Point out each leukocyte.
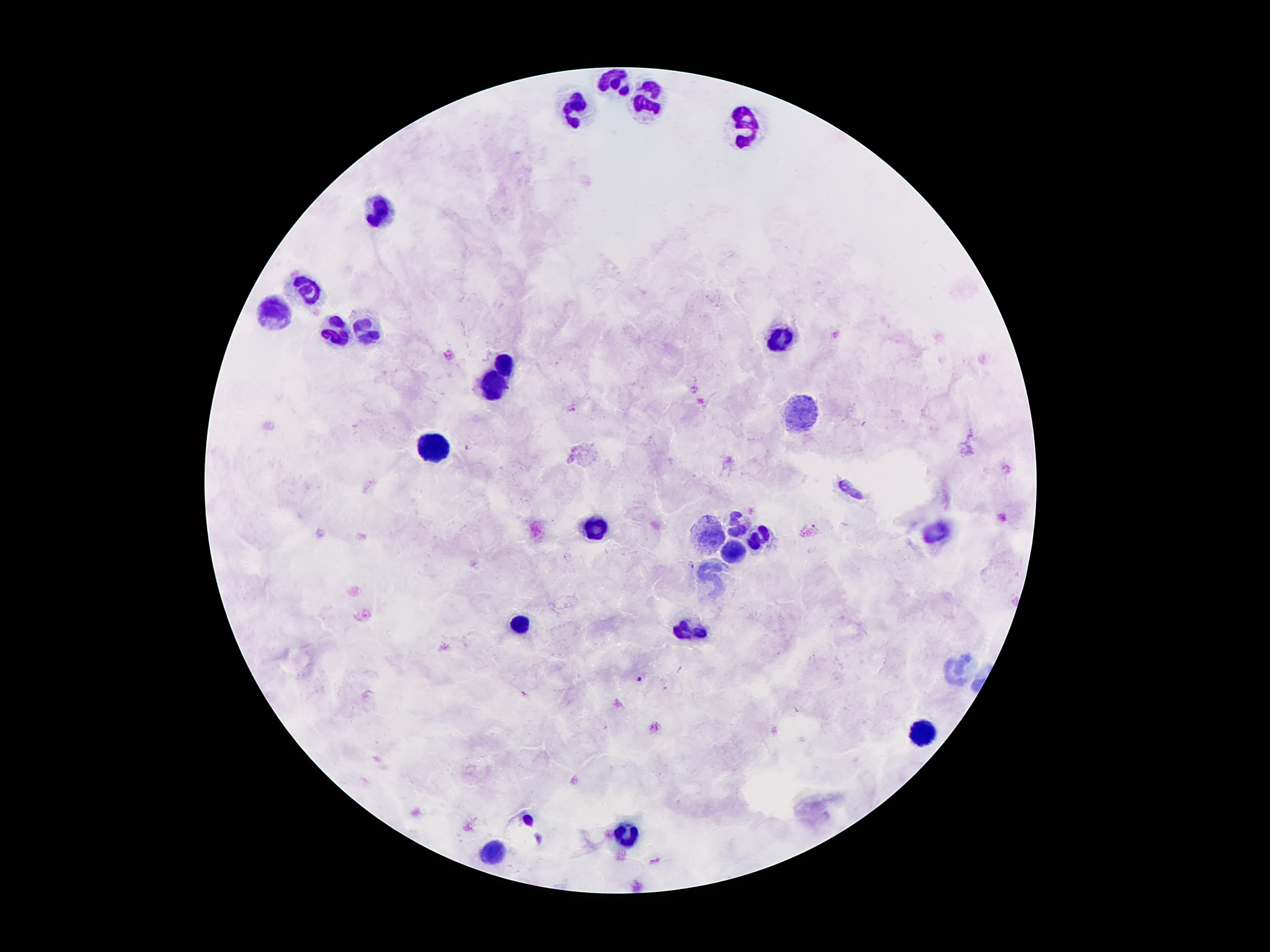
Approximate centers as [x, y] in pixels.
Leukocytes: [617, 81], [646, 104], [579, 106], [741, 129], [380, 211], [306, 288], [275, 314], [363, 325], [336, 331], [779, 337], [506, 364], [495, 387], [806, 414], [434, 448], [735, 524], [596, 528], [938, 533], [707, 535], [754, 541], [730, 552], [712, 578], [521, 626], [688, 632], [955, 669], [924, 731], [626, 832], [493, 853].

Malaria parasite locations: [468, 448], [691, 564], [640, 679]. Patient malaria status: positive for Plasmodium falciparum. Thick blood smear. Single field of view. Giemsa stain. Image is 1270×952 pixels. 100x magnification. Photographed through the microscope eyepiece with a smartphone camera.